Assess this cell for malaria.
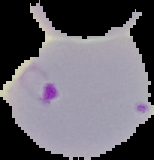
It is parasitized.

Summary:
  - Image size: 154×160 pixels
  - Image type: cell region segmented out of the field of view; surrounding area masked to black
  - Preparation: thin blood smear